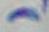

identification: Toxoplasma gondii
magnification: 1000x
modality: photomicrograph